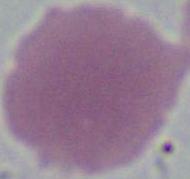

modality = micrograph
magnification = 1000x
identification = red blood cell